Report the malaria status of this cell.
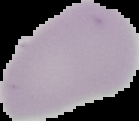
Uninfected.

image type = segmented cell region with the area outside set to black
preparation = thin blood smear
image size = 139×121 pixels